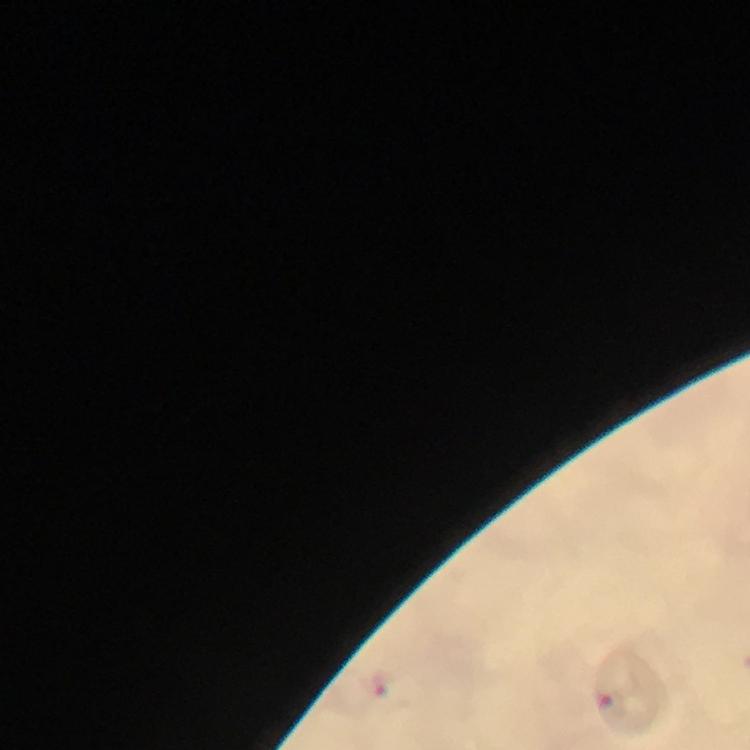
Approximate centers as [x, y] in pixels.
Summary:
  - Malaria parasite locations: [380, 683]
  - Magnification: 100x
  - Preparation: thick blood smear
  - Context: from a malaria diagnostic workup
  - Capture: smartphone photograph through a microscope
  - Stain: Giemsa
  - Image size: 750×750 pixels
  - Immersion oil: used
  - Cropped from: a single field of view